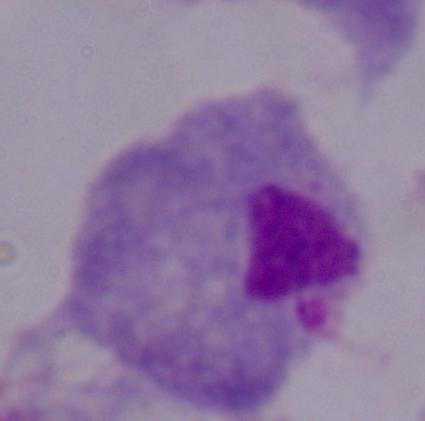 Photomicrograph. 1000x magnification. A trichomonad is seen.